Identify the parasite.
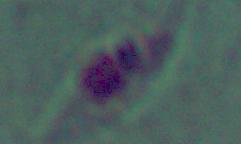

This is Leishmania.

Summary:
  - Magnification: 1000x
  - Modality: micrograph